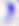
Summary:
  - Magnification: 400x
  - Identification: Toxoplasma gondii
  - Modality: micrograph